Report the malaria status of this cell.
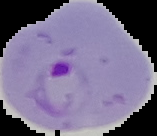

It is parasitized.

Image is 157×136 pixels. From a thin blood smear. Cell region segmented out of the field of view; the surrounding area is masked to black.